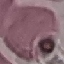 Result: no malaria parasites seen. Acquired by smartphone through the microscope eyepiece. Thin blood smear. Cell patch, automatically extracted from a larger field of view and resized to 64 × 64 pixels. Giemsa-stained preparation.